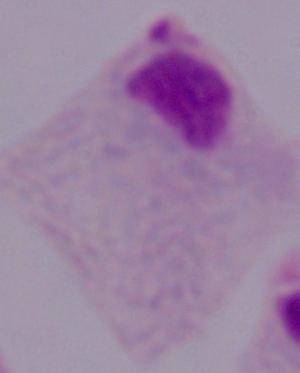
identification: trichomonad
modality: micrograph
magnification: 1000x